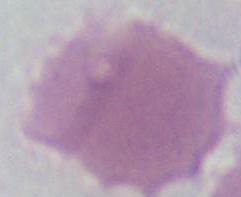 Captured at 1000x magnification. Micrograph. A red blood cell is shown.